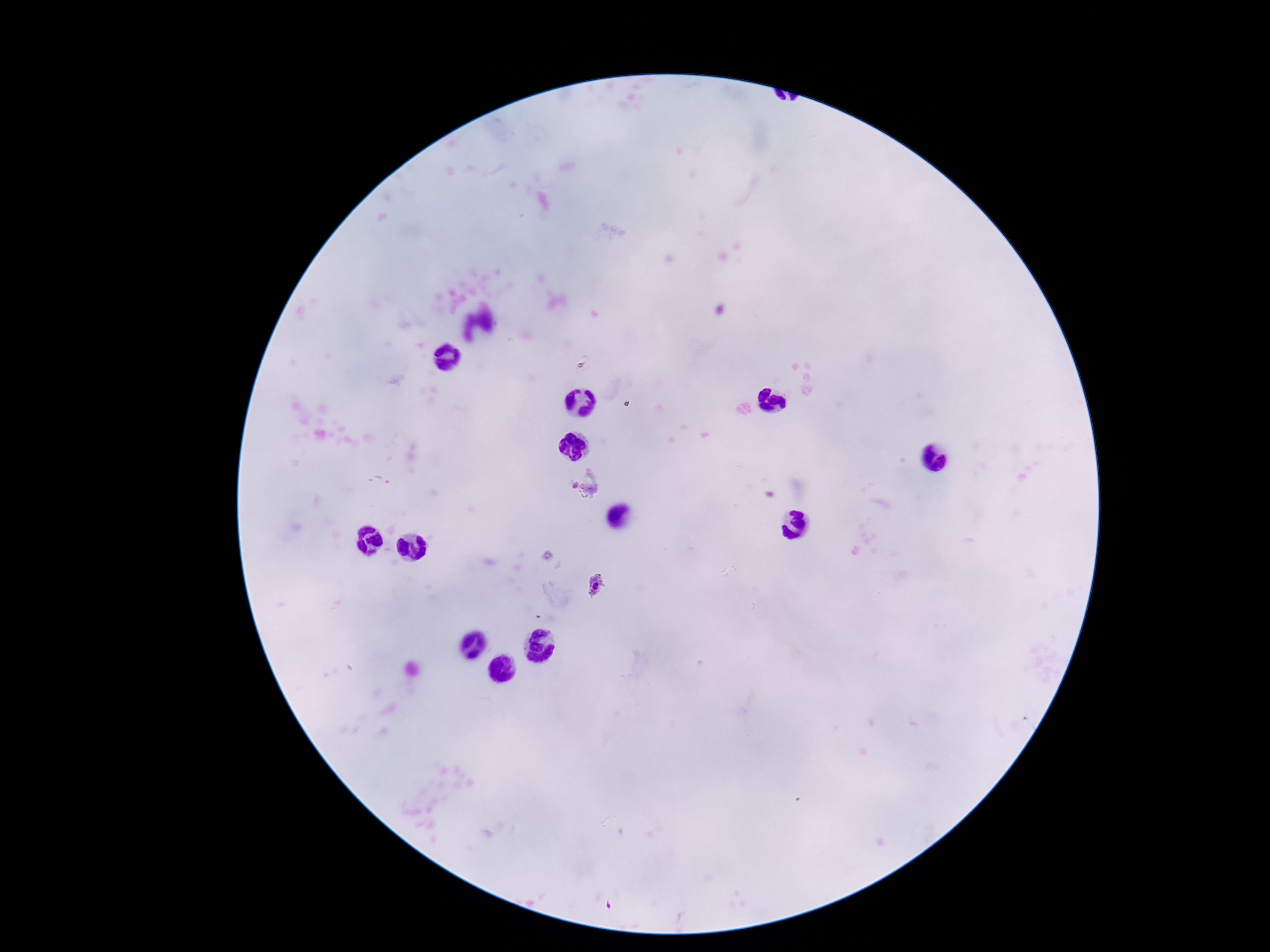
patient malaria status = infected
field of view = single
image size = 1270×952 pixels
magnification = 100x
Plasmodium parasite locations = approximate centers as [x, y] in pixels: [585, 484], [595, 586]
stain = Giemsa
preparation = thick blood film
capture = smartphone camera through the microscope eyepiece